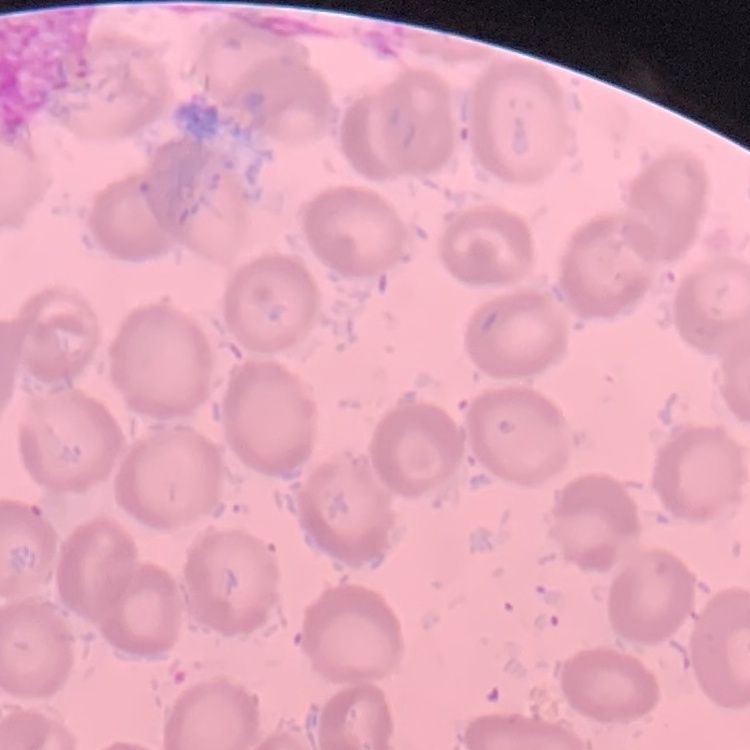

Summary:
  - Erythrocyte morphology: no rouleaux formation
  - Stain: Field's or Giemsa
  - Image type: square crop of a larger photomicrograph
  - Preparation: thin blood film